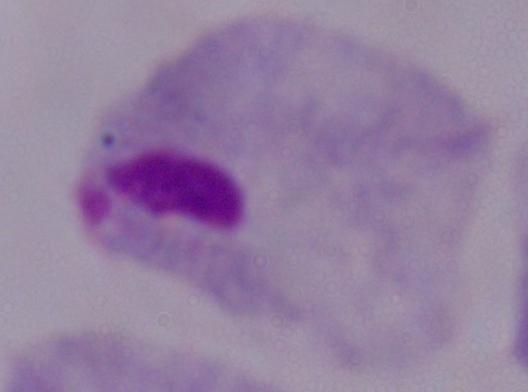
Captured at 1000x magnification. Micrograph. A trichomonad is shown.